Report the malaria status of this cell.
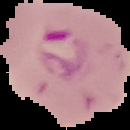

It is parasitized.

Segmented cell region on a black background. From a thin blood film. Image is 130×130 pixels.